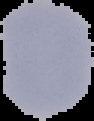
image size = 94×121 pixels
image type = segmented cell region with the area outside set to black
result = no malaria parasites detected
preparation = thin blood film